Outline each blood parasite and name the species.
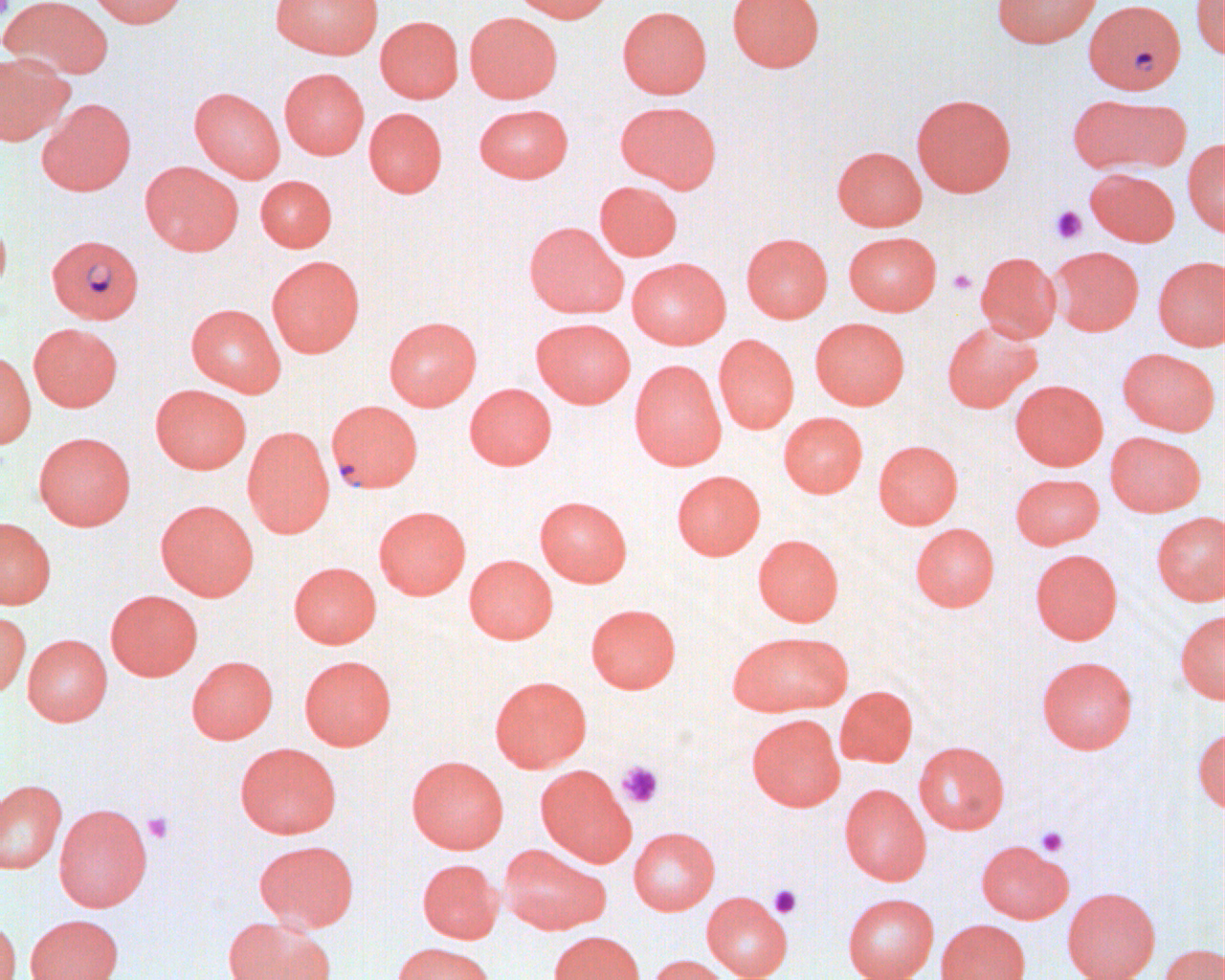

Approximate bounding boxes as named x1/y1/x2/y2 corners in pixels.
Plasmodium falciparum-infected red blood cells: (x1=1084, y1=0, x2=1186, y2=94), (x1=46, y1=234, x2=144, y2=324), (x1=326, y1=400, x2=423, y2=493).
No Plasmodium ovale, Plasmodium malariae, Plasmodium vivax, Babesia divergens, or Trypanosoma brucei observed.

slide-level diagnosis = Plasmodium falciparum
platelet locations = approximate bounding boxes as named x1/y1/x2/y2 corners in pixels: (x1=0, y1=1, x2=13, y2=19), (x1=1050, y1=205, x2=1087, y2=244), (x1=947, y1=268, x2=976, y2=295), (x1=616, y1=760, x2=664, y2=808), (x1=142, y1=812, x2=175, y2=844), (x1=1035, y1=826, x2=1069, y2=857), (x1=768, y1=884, x2=802, y2=919)
field of view = one of a larger specimen
uninfected red blood cell locations = approximate bounding boxes as named x1/y1/x2/y2 corners in pixels: (x1=0, y1=0, x2=112, y2=81), (x1=88, y1=0, x2=188, y2=28), (x1=270, y1=0, x2=383, y2=59), (x1=512, y1=0, x2=613, y2=23), (x1=727, y1=0, x2=825, y2=72), (x1=991, y1=0, x2=1101, y2=48), (x1=1191, y1=0, x2=1225, y2=59), (x1=617, y1=6, x2=711, y2=99), (x1=464, y1=11, x2=562, y2=103), (x1=375, y1=16, x2=464, y2=102), (x1=0, y1=53, x2=71, y2=145), (x1=279, y1=68, x2=369, y2=159), (x1=189, y1=87, x2=285, y2=182), (x1=911, y1=93, x2=1016, y2=197), (x1=1066, y1=94, x2=1178, y2=174), (x1=37, y1=98, x2=137, y2=196), (x1=615, y1=101, x2=722, y2=193), (x1=474, y1=103, x2=573, y2=183), (x1=364, y1=107, x2=447, y2=198), (x1=1182, y1=138, x2=1225, y2=236), (x1=832, y1=145, x2=926, y2=231), (x1=140, y1=161, x2=243, y2=256), (x1=1086, y1=168, x2=1179, y2=246), (x1=255, y1=175, x2=337, y2=252), (x1=594, y1=181, x2=682, y2=260), (x1=0, y1=212, x2=11, y2=301), (x1=524, y1=221, x2=627, y2=318), (x1=843, y1=231, x2=941, y2=315), (x1=741, y1=233, x2=833, y2=322), (x1=1050, y1=246, x2=1143, y2=336), (x1=975, y1=252, x2=1060, y2=342), (x1=266, y1=255, x2=365, y2=357), (x1=1153, y1=256, x2=1225, y2=351), (x1=626, y1=257, x2=730, y2=349), (x1=186, y1=304, x2=286, y2=397), (x1=383, y1=315, x2=482, y2=410), (x1=531, y1=317, x2=636, y2=407), (x1=810, y1=317, x2=910, y2=409), (x1=941, y1=320, x2=1041, y2=412), (x1=28, y1=322, x2=123, y2=412), (x1=714, y1=334, x2=799, y2=433), (x1=1117, y1=348, x2=1219, y2=435), (x1=0, y1=351, x2=35, y2=448), (x1=629, y1=359, x2=727, y2=470), (x1=1010, y1=379, x2=1108, y2=470), (x1=464, y1=383, x2=557, y2=470), (x1=150, y1=384, x2=252, y2=474), (x1=778, y1=411, x2=868, y2=498), (x1=242, y1=426, x2=335, y2=538), (x1=34, y1=431, x2=136, y2=530), (x1=1105, y1=431, x2=1205, y2=516), (x1=873, y1=439, x2=963, y2=528), (x1=671, y1=469, x2=766, y2=560), (x1=1010, y1=473, x2=1104, y2=549), (x1=534, y1=495, x2=632, y2=586), (x1=155, y1=499, x2=259, y2=600), (x1=373, y1=505, x2=471, y2=599), (x1=1151, y1=511, x2=1225, y2=604), (x1=0, y1=517, x2=56, y2=609), (x1=910, y1=523, x2=999, y2=611), (x1=753, y1=534, x2=844, y2=626), (x1=1030, y1=548, x2=1123, y2=644), (x1=464, y1=555, x2=558, y2=644), (x1=288, y1=561, x2=382, y2=648), (x1=105, y1=589, x2=203, y2=680), (x1=586, y1=603, x2=681, y2=693), (x1=1175, y1=609, x2=1225, y2=704), (x1=0, y1=611, x2=31, y2=699), (x1=728, y1=630, x2=853, y2=716), (x1=22, y1=633, x2=113, y2=725), (x1=299, y1=654, x2=397, y2=750), (x1=186, y1=655, x2=278, y2=744), (x1=1037, y1=655, x2=1138, y2=754), (x1=489, y1=675, x2=592, y2=771), (x1=834, y1=685, x2=918, y2=767), (x1=746, y1=713, x2=845, y2=811), (x1=1193, y1=725, x2=1225, y2=814), (x1=913, y1=740, x2=1009, y2=834), (x1=234, y1=742, x2=342, y2=838), (x1=406, y1=755, x2=509, y2=853), (x1=535, y1=764, x2=637, y2=866), (x1=0, y1=779, x2=67, y2=874), (x1=839, y1=784, x2=931, y2=885), (x1=53, y1=803, x2=153, y2=911), (x1=629, y1=826, x2=720, y2=914), (x1=255, y1=839, x2=359, y2=932), (x1=976, y1=839, x2=1073, y2=923), (x1=499, y1=843, x2=610, y2=935), (x1=417, y1=858, x2=504, y2=943), (x1=1062, y1=887, x2=1160, y2=980), (x1=702, y1=891, x2=792, y2=980), (x1=842, y1=893, x2=938, y2=980), (x1=842, y1=912, x2=1032, y2=979), (x1=24, y1=913, x2=123, y2=980), (x1=222, y1=916, x2=333, y2=980), (x1=0, y1=917, x2=21, y2=980), (x1=936, y1=918, x2=1030, y2=980), (x1=548, y1=930, x2=644, y2=980), (x1=393, y1=941, x2=496, y2=980), (x1=1158, y1=943, x2=1225, y2=980), (x1=647, y1=955, x2=732, y2=980)
modality = light microscopy
image size = 1225×980 pixels
preparation = thin blood film
magnification = 1000x